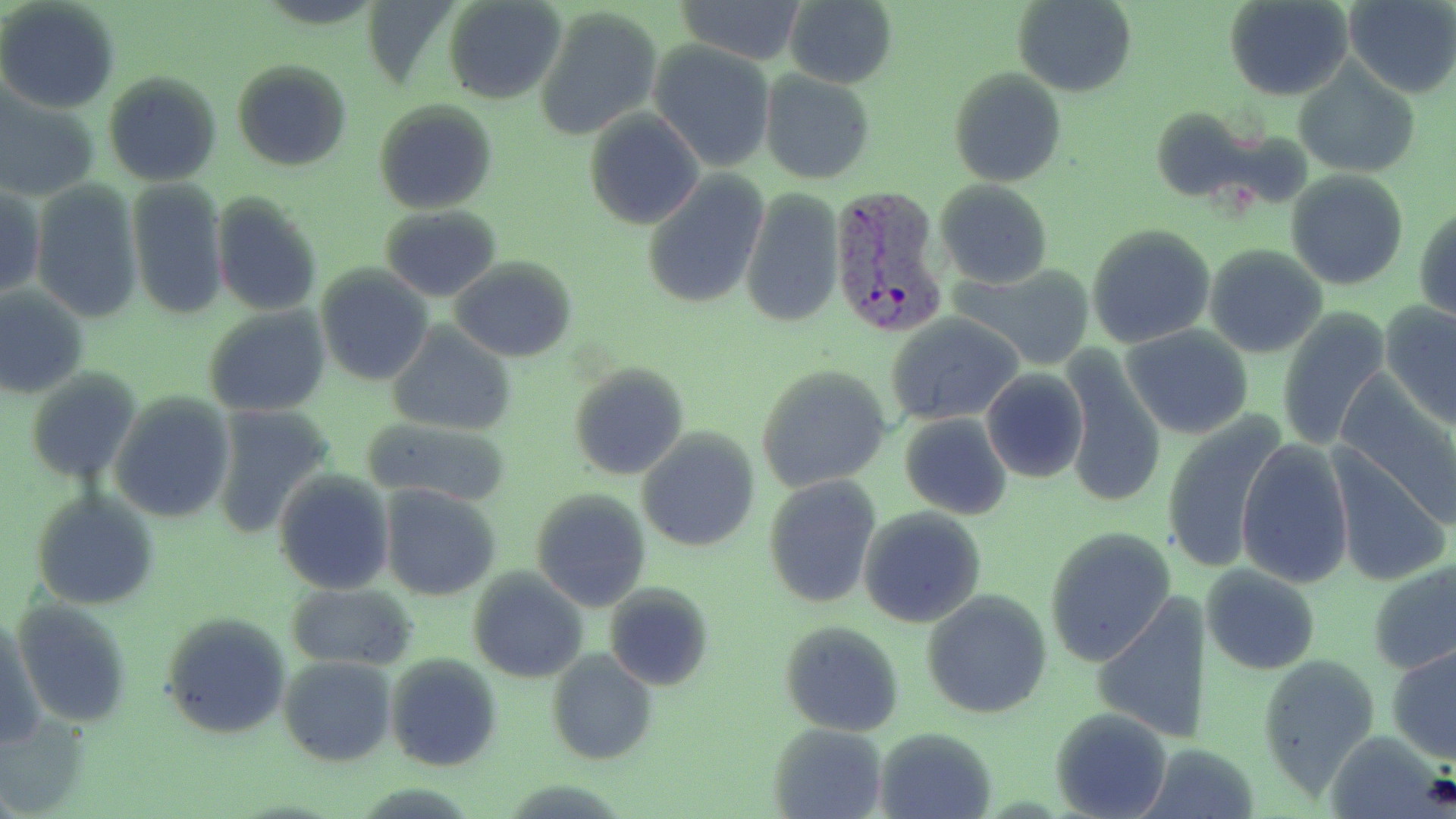

slide-level diagnosis = Plasmodium vivax
preparation = thin blood smear
image size = 1456×819 pixels
Plasmodium vivax-infected red blood cell locations = approximate bounding boxes as (x1,y1)-(x2,y2) corner pairs in pixels: (828,183)-(948,339)
field of view = one of a larger specimen
magnification = 1000x
uninfected red blood cell locations = approximate bounding boxes as (x1,y1)-(x2,y2) corner pairs in pixels: (443,0)-(565,104), (675,0)-(805,65), (786,0)-(898,88), (1014,0)-(1134,97), (1226,0)-(1352,100), (1344,0)-(1456,98), (0,2)-(119,113), (536,6)-(660,139), (650,41)-(778,174), (1293,58)-(1420,181), (231,59)-(352,171), (949,69)-(1066,186), (103,70)-(223,186), (759,72)-(875,185), (0,92)-(99,202), (373,101)-(498,215), (1149,107)-(1256,201), (585,111)-(702,229), (1286,172)-(1410,291), (642,173)-(768,308), (125,180)-(229,321), (935,180)-(1052,288), (30,181)-(142,325), (0,183)-(43,302), (740,186)-(845,329), (212,194)-(321,316), (1415,203)-(1456,324), (380,206)-(503,301), (1086,224)-(1216,349), (1203,243)-(1328,359), (449,257)-(577,362), (951,262)-(1095,370), (316,264)-(433,385), (0,287)-(88,400), (1380,300)-(1456,429), (203,306)-(330,418), (1276,308)-(1393,452), (888,313)-(1025,424), (387,323)-(517,438), (1122,326)-(1253,439), (1059,352)-(1169,508), (569,361)-(687,482), (758,363)-(892,493), (25,367)-(139,483), (981,368)-(1089,485), (1331,385)-(1455,538), (110,395)-(233,523), (210,404)-(334,538), (900,413)-(1013,520), (1162,414)-(1290,578), (361,418)-(510,504), (637,429)-(760,554), (1236,438)-(1354,589), (1326,446)-(1450,588), (273,470)-(395,595), (762,475)-(881,607), (381,485)-(500,601), (531,490)-(651,611), (32,492)-(158,610), (858,508)-(986,629), (1044,527)-(1175,668), (1371,557)-(1455,677), (1201,562)-(1321,675), (468,569)-(586,682), (604,582)-(714,691), (286,583)-(415,669), (922,591)-(1052,720), (1092,594)-(1213,747), (2,611)-(45,750), (161,613)-(293,739), (779,620)-(905,737), (1388,643)-(1456,764), (547,649)-(660,766), (1258,650)-(1382,792), (385,654)-(502,773), (279,656)-(396,766), (1051,706)-(1173,819), (769,723)-(888,818), (876,726)-(997,819)
stain = May-Grünwald-Giemsa
modality = optical microscopy